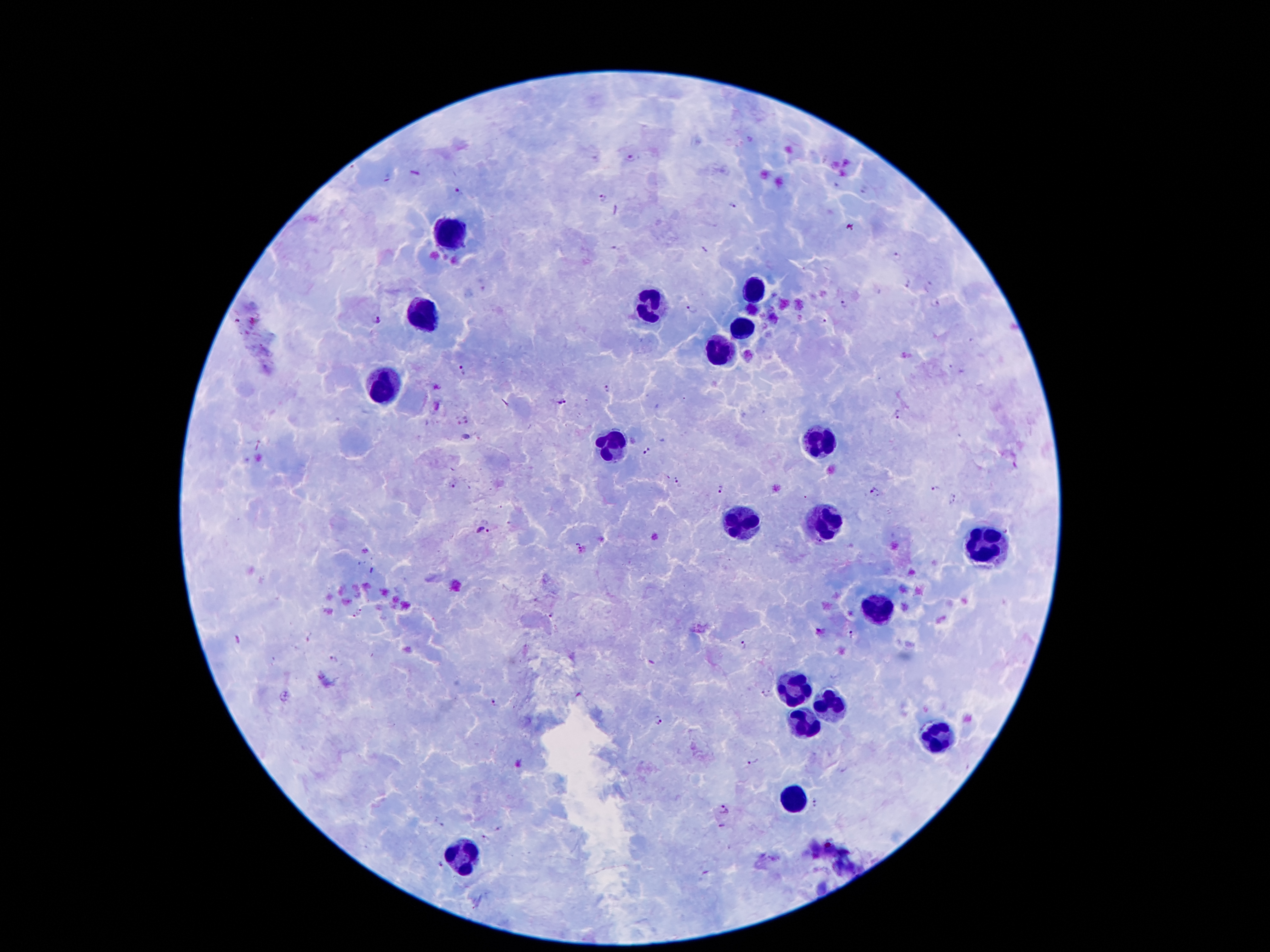
Approximate centers as (x, y) in pixels. Plasmodium parasite locations: (630, 159), (458, 191), (602, 199), (733, 204), (896, 256), (907, 283), (928, 286), (935, 302), (844, 304), (691, 310), (378, 320), (822, 320), (463, 371), (606, 388), (562, 402), (900, 414), (468, 419), (457, 421), (646, 451), (452, 483), (678, 483), (935, 487), (719, 490), (874, 492), (952, 499), (484, 531), (579, 546), (359, 611), (552, 614), (351, 618), (852, 635), (743, 645), (335, 658), (765, 694), (495, 703), (660, 721), (755, 762), (817, 805), (722, 810), (722, 826), (499, 830), (484, 837), (439, 865). Leukocyte locations: (450, 235), (756, 295), (648, 309), (424, 313), (744, 329), (718, 351), (386, 387), (818, 441), (608, 443), (822, 523), (740, 525), (991, 543), (876, 611), (792, 691), (828, 705), (806, 725), (940, 739), (796, 801), (464, 859). One field from this slide. 100x magnification. Image is 1270×952 pixels. Patient malaria status: infected with Plasmodium falciparum. Thick blood film. Smartphone photograph taken through the microscope eyepiece. Giemsa stain.